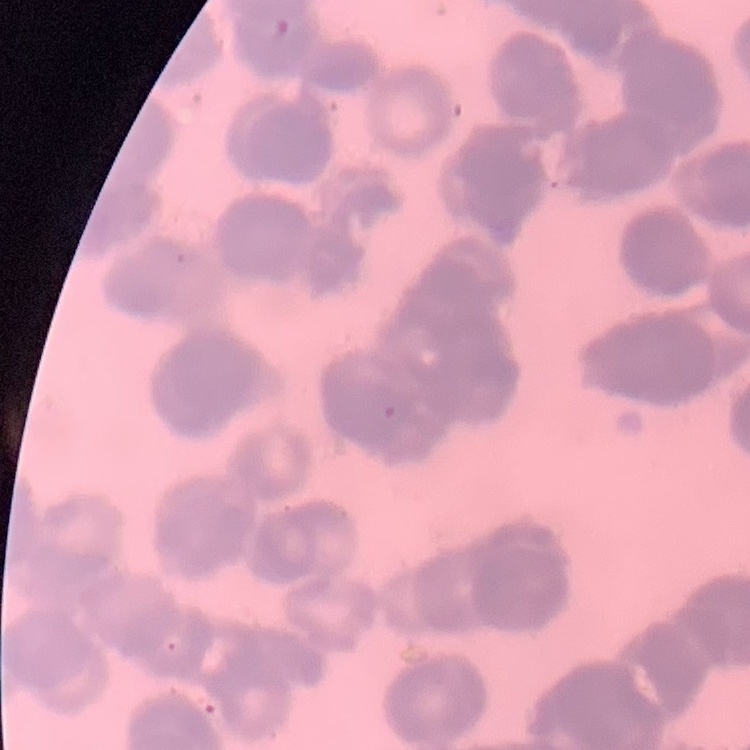 The erythrocytes exhibit rouleaux formation. Square crop of a larger photomicrograph. Stained with either Field's or Giemsa. Thin blood film.